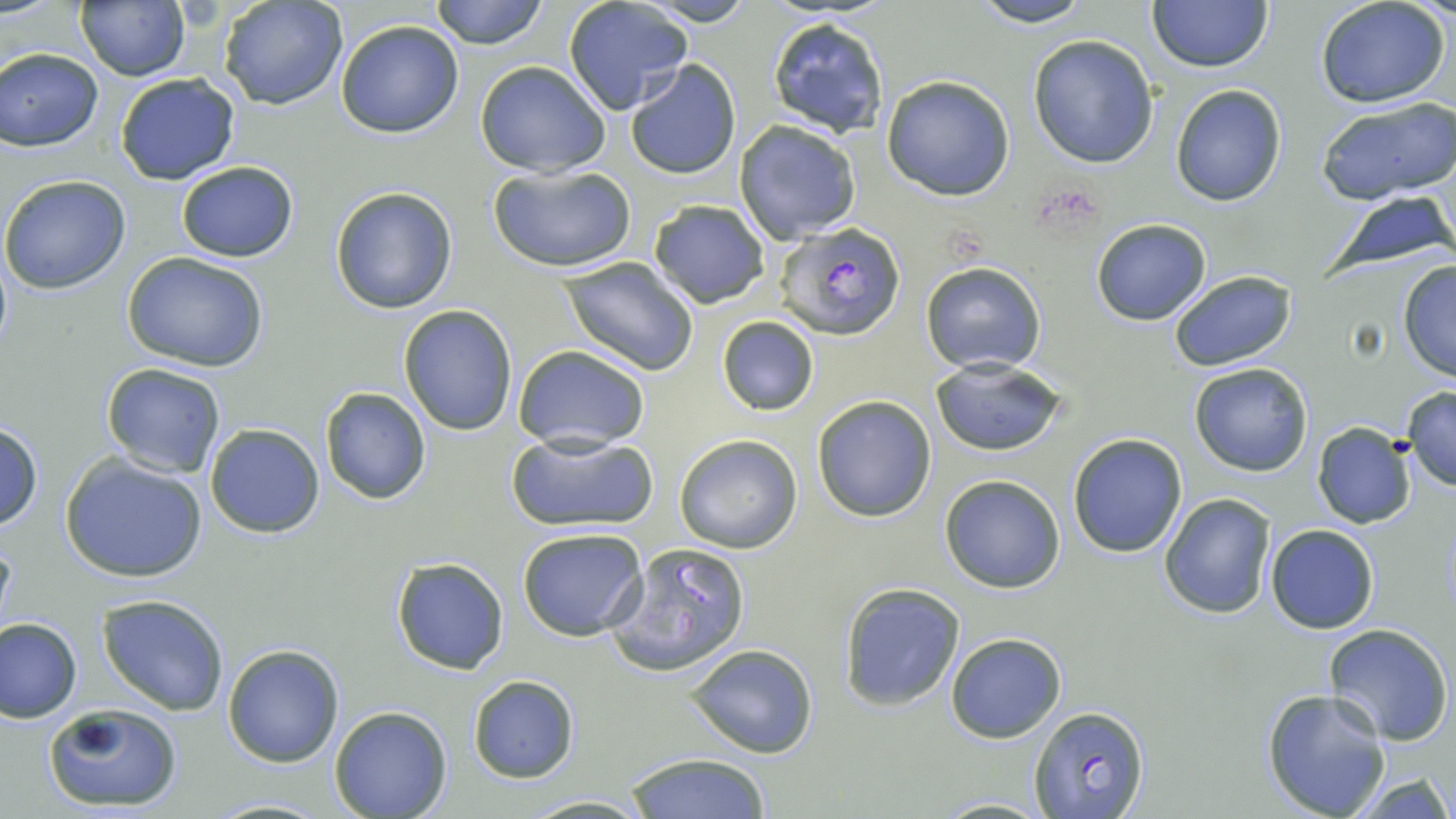

{
  "slide_level_diagnosis": "Plasmodium falciparum",
  "preparation": "thin blood smear",
  "modality": "light microscopy",
  "image_size": "1456×819 pixels",
  "plasmodium_falciparum_infected_red_blood_cell_locations": "approximate bounding boxes as (x1, y1, x2, y2) in pixels: (774, 222, 906, 340)",
  "field_of_view": "one of a larger specimen",
  "stain": "May-Grünwald-Giemsa",
  "magnification": "1000x",
  "uninfected_red_blood_cell_locations": "approximate bounding boxes as (x1, y1, x2, y2) in pixels: (218, 0, 349, 110), (428, 0, 548, 49), (965, 0, 1095, 28), (562, 1, 692, 115), (638, 1, 758, 27), (1146, 1, 1272, 73), (1315, 1, 1454, 110), (76, 2, 190, 81), (765, 15, 890, 138), (334, 19, 464, 139), (1028, 36, 1159, 168), (0, 47, 104, 151), (475, 60, 610, 177), (625, 60, 742, 181), (114, 73, 242, 186), (882, 75, 1014, 200), (1170, 84, 1286, 207), (1315, 96, 1456, 204), (733, 120, 861, 243), (176, 161, 298, 263), (489, 165, 637, 274), (0, 174, 132, 294), (330, 187, 459, 314), (1321, 189, 1456, 276), (648, 200, 769, 308), (1091, 218, 1212, 326), (125, 253, 269, 371), (560, 258, 700, 375), (1395, 259, 1456, 382), (920, 261, 1046, 374), (1168, 271, 1295, 372), (398, 306, 518, 436), (717, 315, 819, 417), (513, 344, 651, 453), (930, 359, 1067, 456), (1188, 362, 1313, 476), (101, 363, 228, 478), (1400, 386, 1456, 492), (318, 387, 432, 505), (811, 394, 937, 522), (0, 421, 43, 531), (204, 423, 326, 537), (1312, 423, 1416, 529), (507, 430, 657, 532), (1066, 433, 1187, 558), (674, 434, 802, 553), (57, 453, 211, 585), (940, 474, 1066, 594), (1159, 492, 1277, 618), (1265, 524, 1379, 633), (516, 527, 650, 642), (1, 535, 16, 644), (607, 542, 752, 676), (390, 557, 509, 675), (837, 582, 966, 709), (99, 595, 229, 716), (1, 617, 82, 723), (1323, 624, 1453, 747), (946, 633, 1066, 743), (223, 644, 344, 767), (686, 644, 819, 759), (468, 676, 578, 782), (1262, 689, 1392, 818), (42, 703, 181, 813), (330, 706, 452, 819), (1028, 706, 1149, 818), (621, 751, 775, 818), (1353, 774, 1455, 817), (519, 793, 655, 817), (205, 797, 335, 817), (932, 798, 1057, 818)"
}